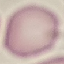

Result: no malaria parasites detected. Giemsa stain. Automatically extracted cell patch, resized to 64 × 64 pixels. Thin blood film. Photographed with a smartphone camera at the microscope eyepiece.